State which parasite is depicted.
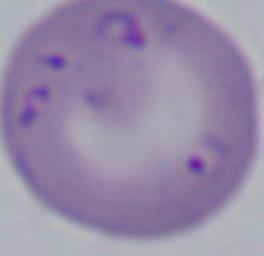
This is Babesia.

modality: photomicrograph
magnification: 1000x